Name the parasite shown.
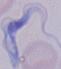
This is a trypanosome.

Captured at 1000x magnification. Micrograph.